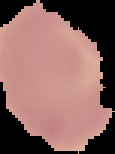

Image is 115×154 pixels. Result: no malaria parasites seen. Cell region segmented out of the field of view; the surrounding area is masked to black. From a thin blood film.